Give the extent of all uninfected red blood cells.
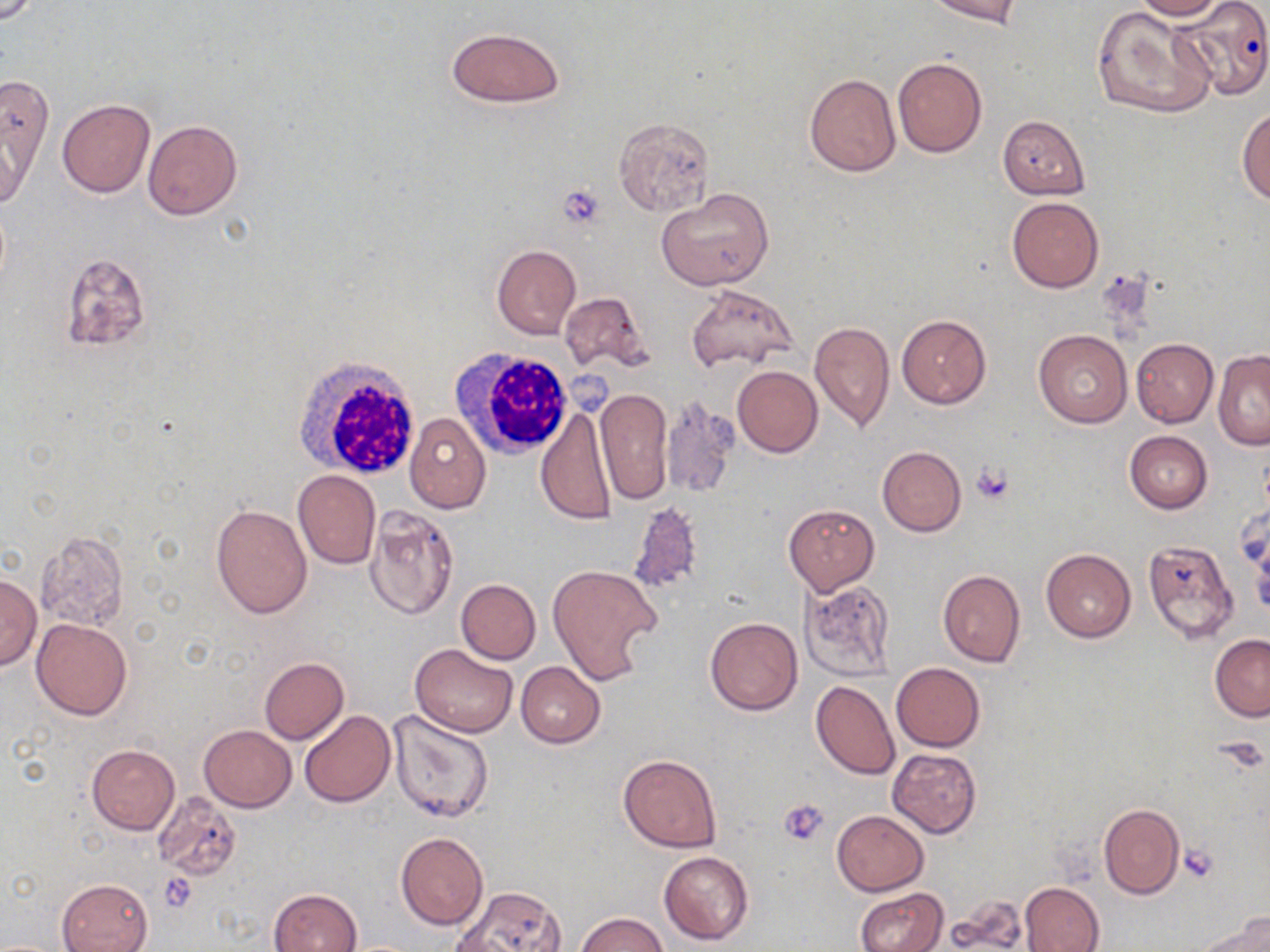
Approximate bounding boxes as [x1, y1, x2, y2] in pixels.
Uninfected red blood cells: [927, 0, 1021, 25], [1132, 0, 1225, 20], [1172, 3, 1268, 103], [1090, 5, 1216, 120], [445, 26, 564, 108], [893, 57, 987, 158], [805, 72, 900, 176], [1, 75, 53, 197], [57, 99, 154, 198], [1238, 109, 1270, 203], [997, 115, 1090, 199], [613, 117, 714, 216], [143, 119, 243, 221], [657, 187, 774, 291], [1006, 196, 1103, 292], [492, 244, 580, 339], [60, 251, 151, 352], [686, 282, 796, 375], [559, 291, 652, 375], [896, 315, 991, 408], [808, 321, 894, 431], [1034, 330, 1132, 427], [1131, 338, 1218, 428], [1212, 351, 1270, 450], [732, 366, 823, 457], [593, 388, 672, 503], [661, 398, 739, 497], [536, 406, 618, 525], [405, 414, 491, 513], [1124, 431, 1213, 513], [877, 446, 966, 535], [293, 470, 381, 569], [628, 500, 706, 597], [211, 504, 312, 618], [783, 504, 880, 595], [364, 506, 459, 620], [591, 508, 698, 636], [34, 530, 131, 633], [1143, 541, 1240, 646], [1041, 548, 1136, 642], [548, 564, 662, 688], [938, 569, 1025, 667], [0, 575, 41, 670], [800, 578, 896, 682], [455, 579, 541, 664], [705, 616, 803, 716], [32, 619, 132, 719], [1210, 634, 1270, 721], [410, 644, 519, 737], [259, 658, 349, 744], [516, 661, 605, 748], [891, 662, 985, 752], [812, 680, 900, 780], [385, 709, 494, 824], [298, 710, 394, 807], [199, 724, 296, 811], [86, 744, 180, 833], [887, 749, 982, 837], [618, 753, 723, 854], [154, 792, 243, 880], [1099, 804, 1184, 899], [832, 810, 928, 895], [396, 833, 488, 930], [658, 850, 754, 945], [57, 877, 153, 952], [1019, 882, 1105, 952], [455, 886, 565, 951], [855, 887, 947, 952], [268, 888, 361, 952], [948, 897, 1030, 948], [575, 911, 668, 952], [1200, 914, 1270, 952].

{
  "slide_level_diagnosis": "negative for blood parasites",
  "stain": "May-Grünwald-Giemsa",
  "preparation": "thin blood smear",
  "platelet_locations": "approximate bounding boxes as [x1, y1, x2, y2] in pixels: [556, 184, 606, 229], [971, 462, 1016, 505], [1217, 736, 1266, 776], [779, 798, 828, 846], [1180, 845, 1220, 885], [159, 874, 199, 912]",
  "field_of_view": "one of a larger specimen",
  "modality": "light microscopy",
  "image_size": "1270×952 pixels",
  "white_blood_cell_locations": "approximate bounding boxes as [x1, y1, x2, y2] in pixels: [452, 347, 577, 459], [291, 353, 423, 481]",
  "magnification": "1000x"
}